Identify the parasite.
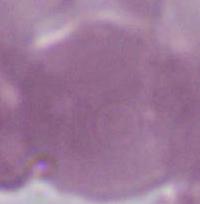

This is Plasmodium.

400x or 1000x magnification. Micrograph.